Evaluate for malaria.
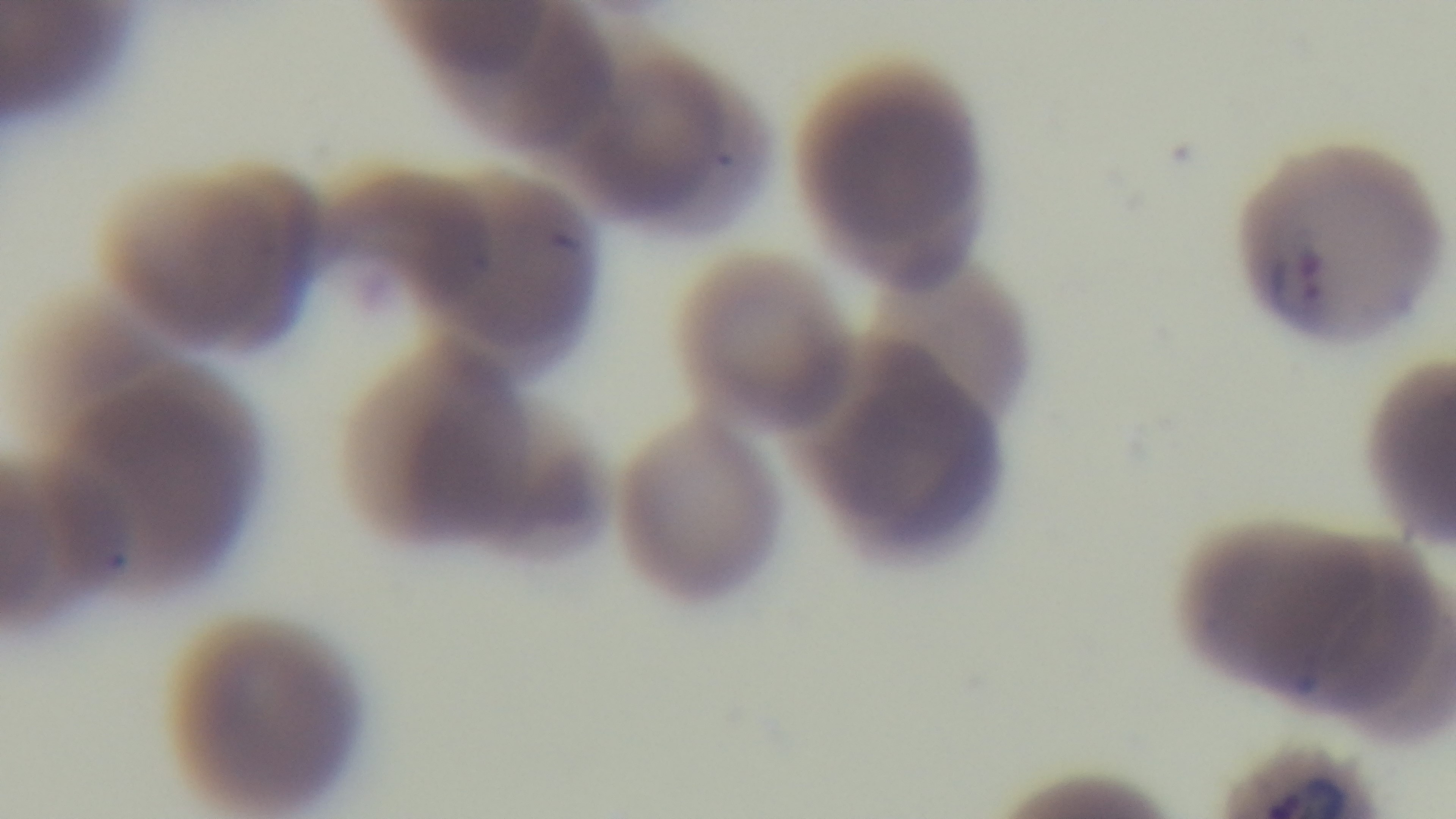
Positive.

Summary:
  - Modality: light microscopy
  - Field of view: one from the slide
  - Capture: mounted 4K digital camera
  - Objective: 100x oil immersion
  - Preparation: thin smear
  - Stain: Giemsa